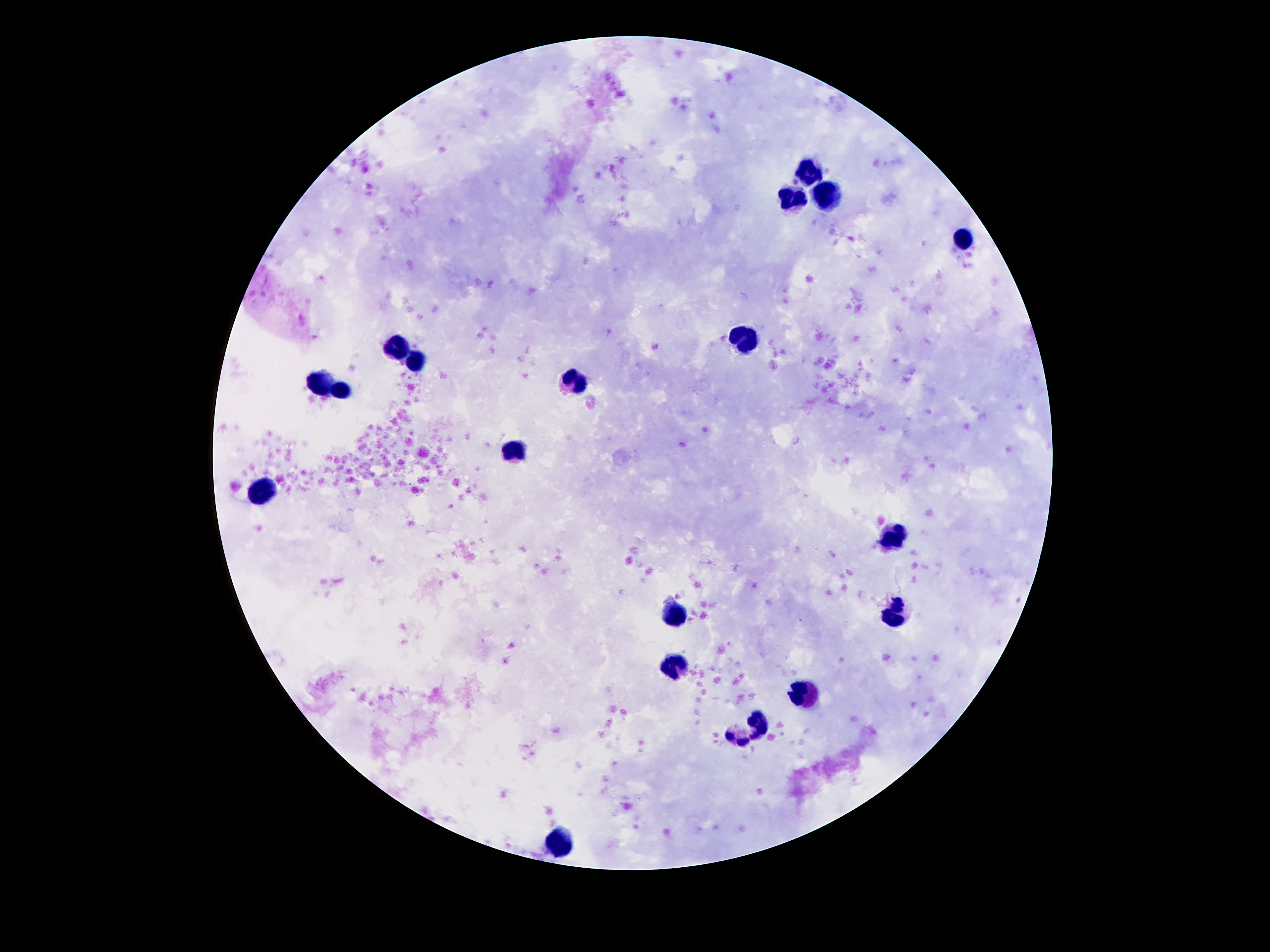

capture = smartphone camera through the microscope eyepiece
preparation = thick blood film
field of view = one from this slide
patient malaria status = uninfected
stain = Giemsa
magnification = 100x
leukocyte locations = approximate object centers, in pixels from the top-left corner: (x=808, y=172), (x=824, y=195), (x=790, y=196), (x=965, y=241), (x=747, y=336), (x=399, y=350), (x=417, y=364), (x=574, y=377), (x=320, y=385), (x=345, y=390), (x=515, y=452), (x=265, y=493), (x=897, y=535), (x=896, y=614), (x=678, y=616), (x=678, y=669), (x=808, y=694), (x=760, y=722), (x=739, y=739), (x=561, y=840)
image size = 1270×952 pixels